State which parasite is depicted.
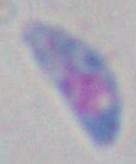
This is Toxoplasma gondii.

magnification: 1000x
modality: micrograph